Identify the cell.
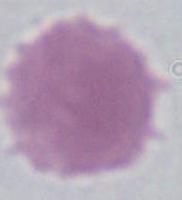
This is an erythrocyte.

modality: photomicrograph
magnification: 1000x